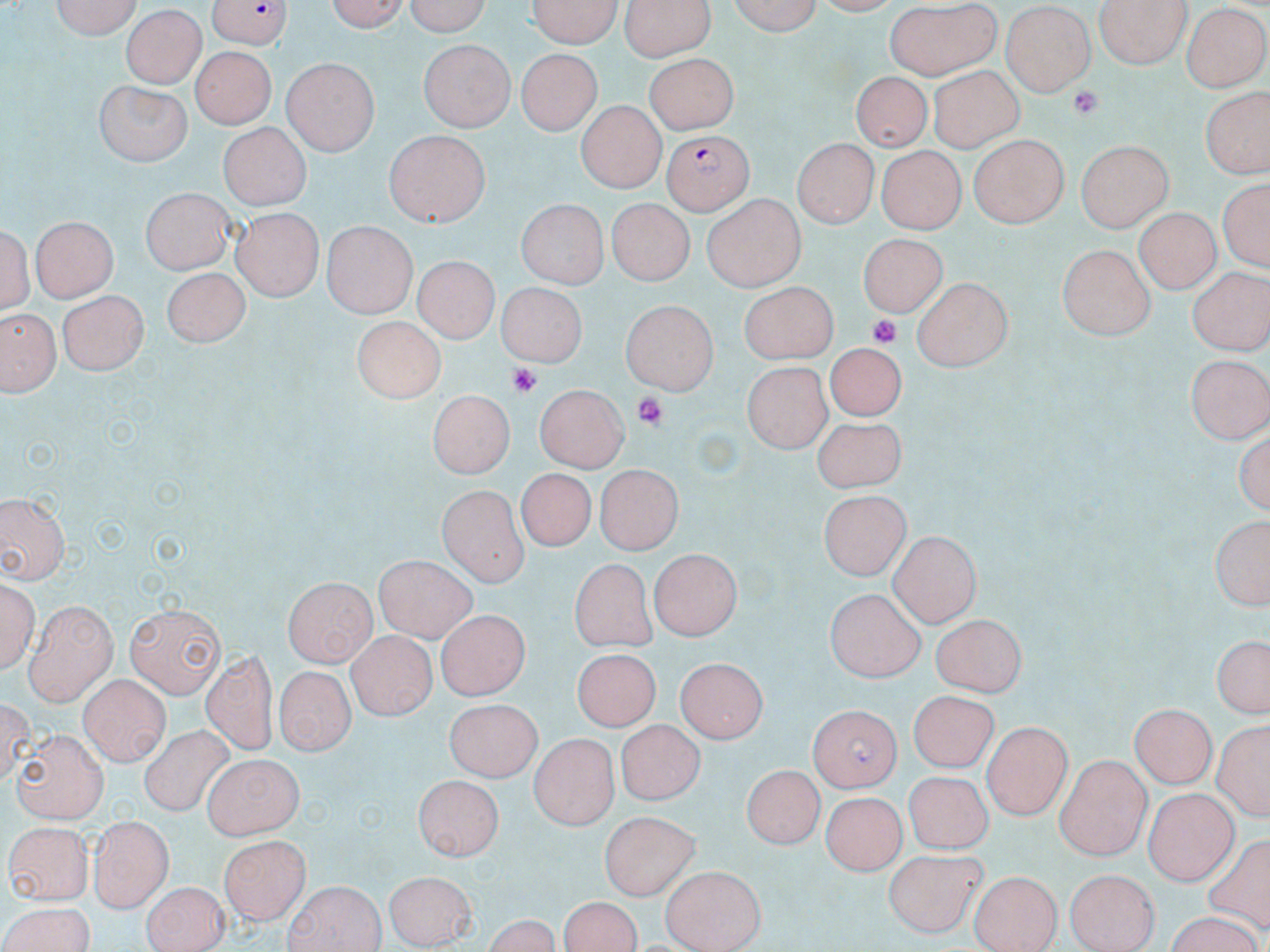
Approximate bounding boxes as (x1,y1)-(x2,y2) corner pairs in pixels. Plasmodium falciparum-infected red blood cell locations: (204,0)-(294,49), (664,129)-(752,213). Uninfected red blood cell locations: (51,0)-(141,39), (324,0)-(415,32), (399,0)-(495,32), (527,0)-(626,49), (623,0)-(714,61), (721,0)-(824,34), (1094,0)-(1193,68), (886,5)-(1002,76), (1000,6)-(1096,96), (1182,6)-(1269,90), (119,7)-(209,88), (420,39)-(513,130), (190,47)-(273,129), (519,48)-(602,133), (647,51)-(738,135), (283,58)-(376,157), (926,66)-(1026,148), (849,71)-(934,152), (95,79)-(193,165), (1204,92)-(1267,178), (575,103)-(664,193), (216,122)-(305,210), (383,130)-(491,229), (968,134)-(1071,228), (793,138)-(876,229), (1077,139)-(1174,232), (876,149)-(966,232), (1217,175)-(1268,277), (136,184)-(232,272), (161,191)-(248,314), (699,194)-(806,289), (514,197)-(611,286), (608,202)-(694,286), (232,206)-(324,302), (1132,208)-(1217,294), (34,214)-(117,302), (2,219)-(35,318), (320,222)-(417,315), (858,232)-(949,318), (1056,242)-(1153,340), (413,255)-(495,342), (1187,262)-(1268,354), (162,265)-(252,348), (913,277)-(1008,371), (738,280)-(836,361), (496,281)-(584,365), (56,288)-(149,378), (618,300)-(718,397), (2,312)-(56,394), (353,320)-(444,402), (826,341)-(907,418), (1185,354)-(1270,444), (743,359)-(834,451), (532,384)-(628,472), (425,387)-(513,478), (815,423)-(906,492), (1234,423)-(1270,517), (519,468)-(591,551), (594,468)-(683,554), (438,483)-(527,586), (0,490)-(70,583), (816,493)-(911,581), (1207,513)-(1270,614), (892,531)-(980,629), (652,547)-(745,638), (376,555)-(473,642), (566,562)-(652,653), (0,577)-(40,678), (283,577)-(377,667), (824,588)-(928,682), (22,601)-(116,705), (126,602)-(225,697), (435,612)-(525,700), (931,612)-(1028,692), (345,629)-(430,721), (1208,633)-(1269,721), (577,647)-(657,726), (203,650)-(275,756), (674,658)-(767,741), (276,667)-(351,757), (80,675)-(171,764), (912,689)-(996,762), (447,702)-(541,780), (1129,703)-(1217,788), (807,704)-(909,790), (1210,717)-(1268,824), (614,719)-(705,803), (984,721)-(1070,819), (139,727)-(240,819), (10,731)-(108,820), (528,734)-(618,828), (203,752)-(301,836), (1054,753)-(1153,858), (744,762)-(823,846), (902,769)-(995,852), (415,777)-(502,862), (1145,789)-(1237,884), (817,795)-(901,875), (599,811)-(700,899), (86,816)-(173,911), (3,823)-(89,907), (218,835)-(309,925), (884,847)-(985,938), (660,864)-(766,952), (1063,866)-(1160,952), (967,868)-(1062,952), (383,871)-(478,945), (142,879)-(226,952), (283,880)-(384,951), (560,898)-(640,951), (0,901)-(97,952), (1159,915)-(1266,952). Platelet locations: (1069,87)-(1103,118), (866,316)-(905,349), (506,362)-(542,395), (633,393)-(668,427). Slide-level diagnosis: Plasmodium falciparum. Captured at 1000x magnification. May-Grünwald-Giemsa-stained preparation. One field of a larger specimen. Thin blood film. Image is 1270×952 pixels. Optical microscopy.